Describe the morphology of the red blood cells.
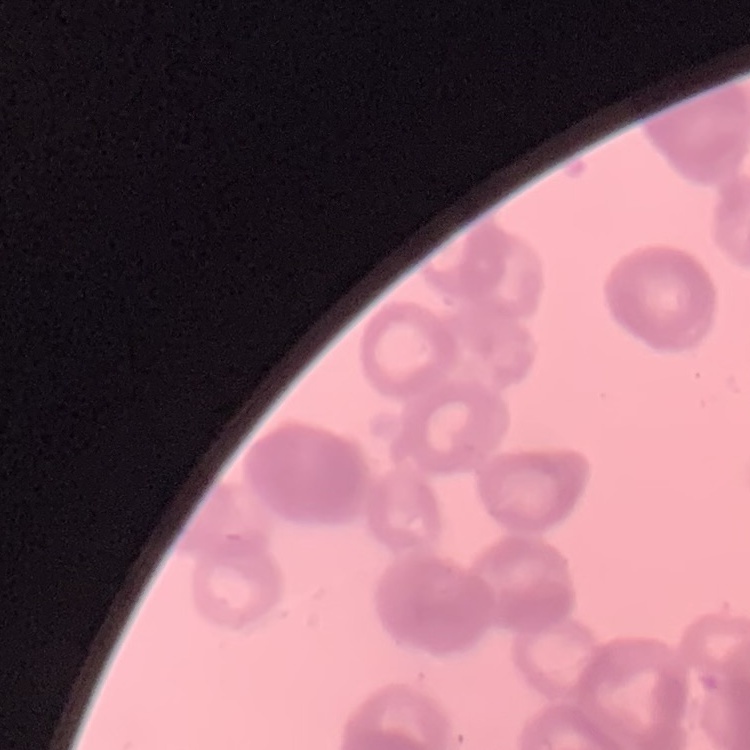
They show rouleaux formation.

preparation = thin peripheral smear
image type = square crop of a larger photomicrograph
stain = Field's or Giemsa